Locate every blood parasite and identify its species.
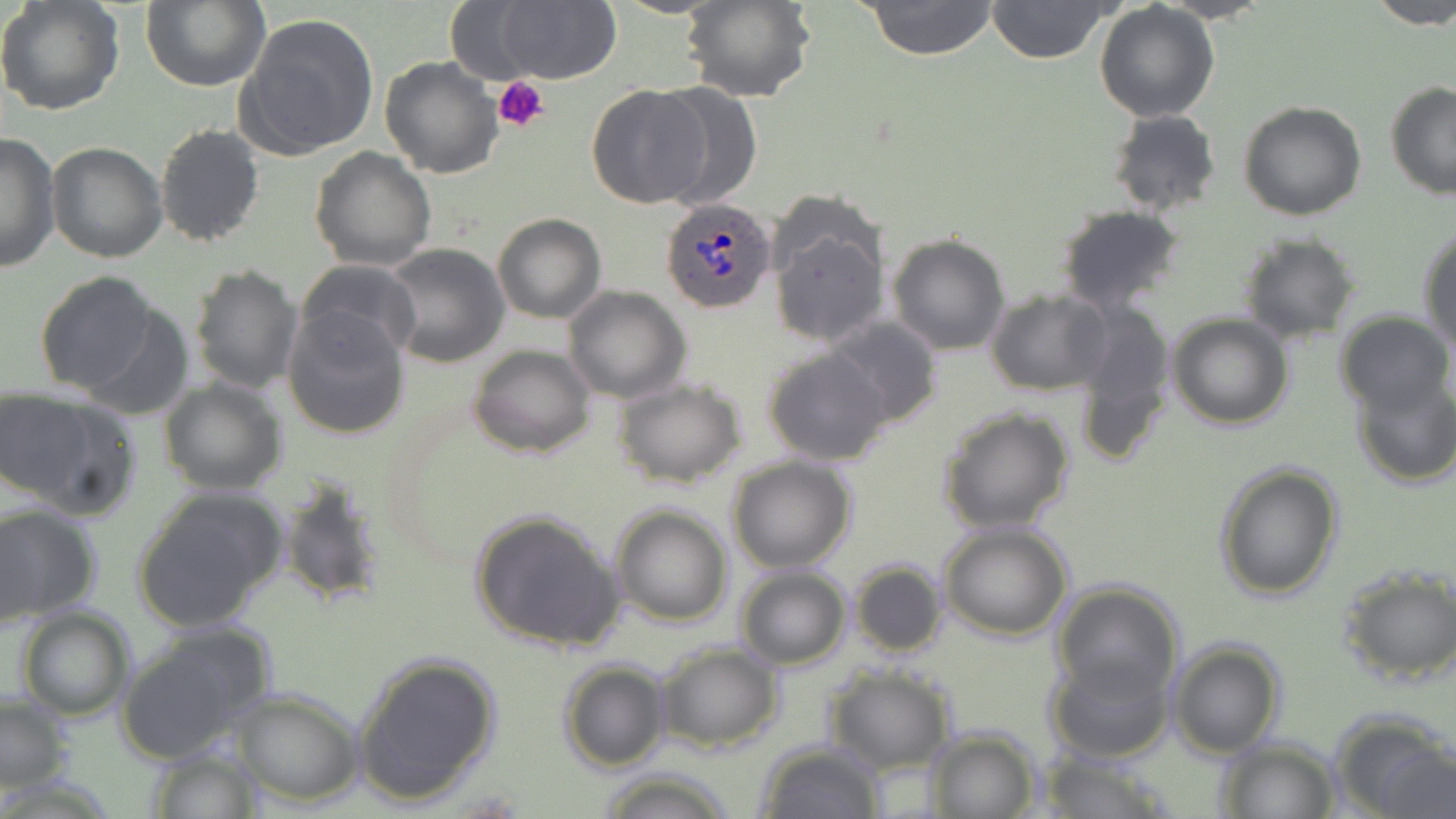
Approximate bounding boxes as (x1,y1)-(x2,y2) corner pairs in pixels.
Plasmodium ovale-infected red blood cells: (659,196)-(776,313).
No Plasmodium falciparum, Plasmodium malariae, Plasmodium vivax, Babesia divergens, or Trypanosoma brucei observed.

Platelet locations: (492,76)-(549,133). Uninfected red blood cell locations: (0,0)-(126,117), (139,0)-(270,92), (609,0)-(728,19), (681,0)-(814,103), (861,0)-(1000,59), (987,0)-(1112,65), (1368,0)-(1456,30), (1094,2)-(1220,121), (444,3)-(546,83), (493,3)-(619,85), (237,13)-(379,160), (378,54)-(503,179), (1385,80)-(1456,198), (586,83)-(712,209), (649,83)-(763,208), (1238,101)-(1367,221), (1107,109)-(1221,216), (155,122)-(265,247), (0,131)-(59,273), (45,142)-(167,262), (310,145)-(436,269), (765,205)-(888,350), (1053,206)-(1186,314), (493,212)-(606,323), (1419,227)-(1456,350), (1238,233)-(1363,344), (887,235)-(1012,355), (381,243)-(511,368), (518,254)-(637,392), (296,258)-(421,364), (188,264)-(302,394), (34,272)-(163,396), (563,286)-(692,403), (985,289)-(1112,396), (1073,299)-(1175,460), (69,301)-(193,418), (283,306)-(410,440), (1334,310)-(1452,415), (1168,312)-(1292,429), (824,317)-(944,428), (469,345)-(596,459), (763,346)-(891,465), (1350,374)-(1456,489), (612,378)-(748,488), (159,379)-(287,495), (1,392)-(136,517), (936,406)-(1076,533), (727,456)-(855,573), (1214,461)-(1343,602), (277,477)-(389,609), (131,488)-(287,632), (0,504)-(101,625), (609,504)-(733,627), (469,508)-(626,654), (938,523)-(1074,641), (849,558)-(948,658), (1338,566)-(1456,685), (735,568)-(851,669), (1050,580)-(1185,705), (13,605)-(136,720), (114,623)-(276,765), (1168,638)-(1286,758), (654,641)-(783,751), (350,652)-(502,805), (1046,653)-(1176,765), (557,659)-(670,771), (827,668)-(956,773), (231,688)-(365,804), (1,694)-(73,793), (1331,709)-(1455,819), (919,727)-(1040,817), (1212,739)-(1341,818), (1382,742)-(1455,818), (755,743)-(886,819), (147,748)-(265,818), (1036,750)-(1172,819), (597,767)-(735,819). Slide-level diagnosis: Plasmodium ovale. 1000x magnification. May-Grünwald-Giemsa-stained preparation. Single field of view. Thin blood film. Optical microscopy. Image is 1456×819 pixels.